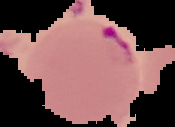

malaria_status: parasitized
image_type: cell region segmented out of the field of view; surrounding area masked to black
preparation: thin blood smear
image_size: 175×127 pixels